Classify this cell by malaria status.
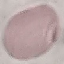

Uninfected.

Automatically extracted cell patch, resized to 64 × 64 pixels. Thin blood film. Giemsa stain. Photographed with a smartphone camera at the microscope eyepiece.